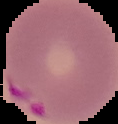

preparation = thin blood film
image size = 118×124 pixels
malaria status = parasitized
image type = segmented cell region on a black background